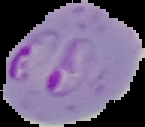
Summary:
  - Image size: 145×127 pixels
  - Preparation: thin blood film
  - Image type: segmented cell region with the area outside set to black
  - Malaria status: parasitized